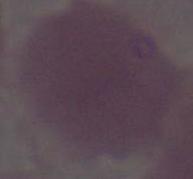
Summary:
  - Identification: erythrocyte
  - Magnification: 1000x
  - Modality: photomicrograph